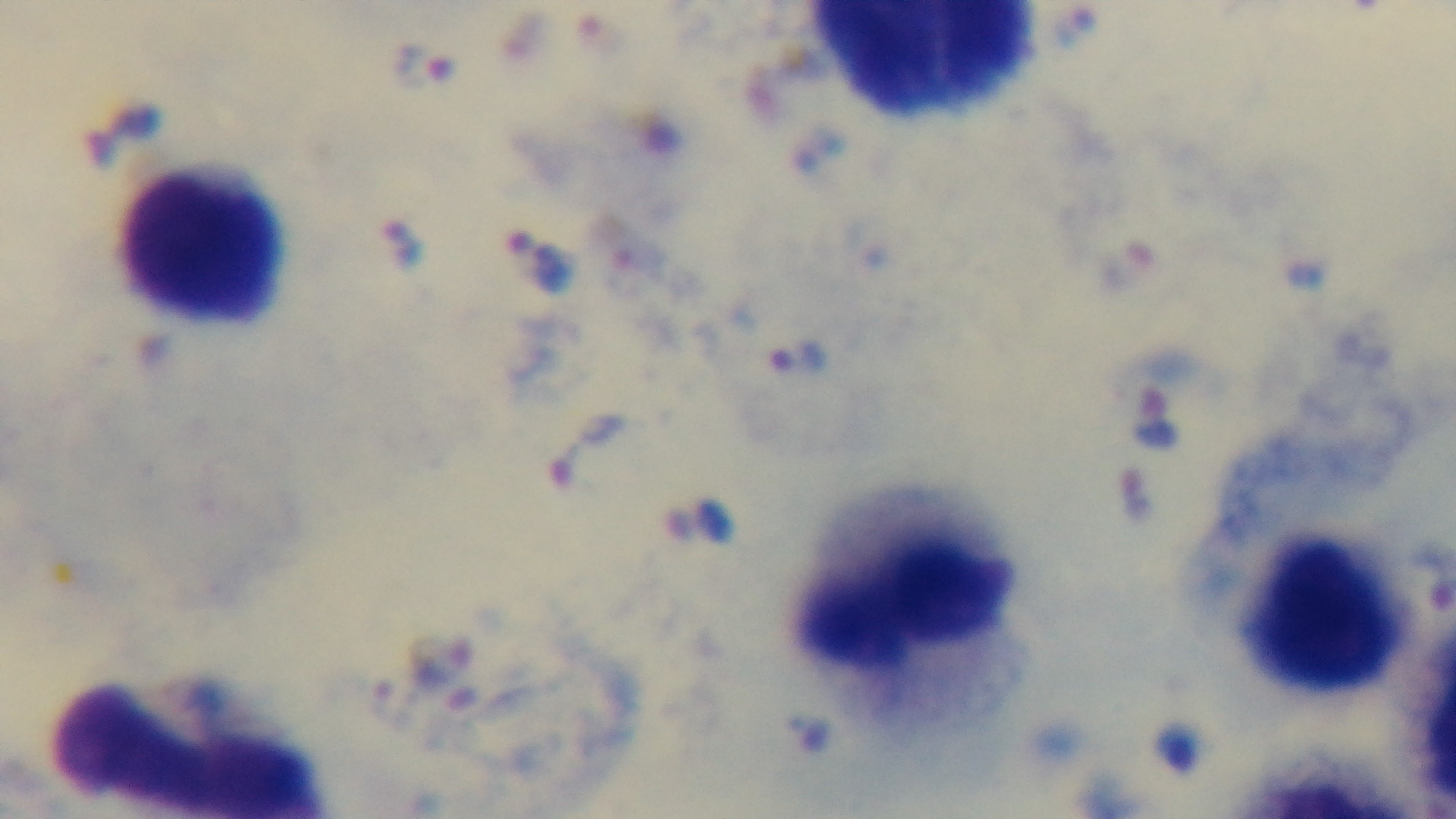 Preparation: thick smear. 100x oil-immersion objective. Malaria status: infected. Giemsa stain. Captured with a mounted 4K digital camera. One field from the slide. Photomicrograph.